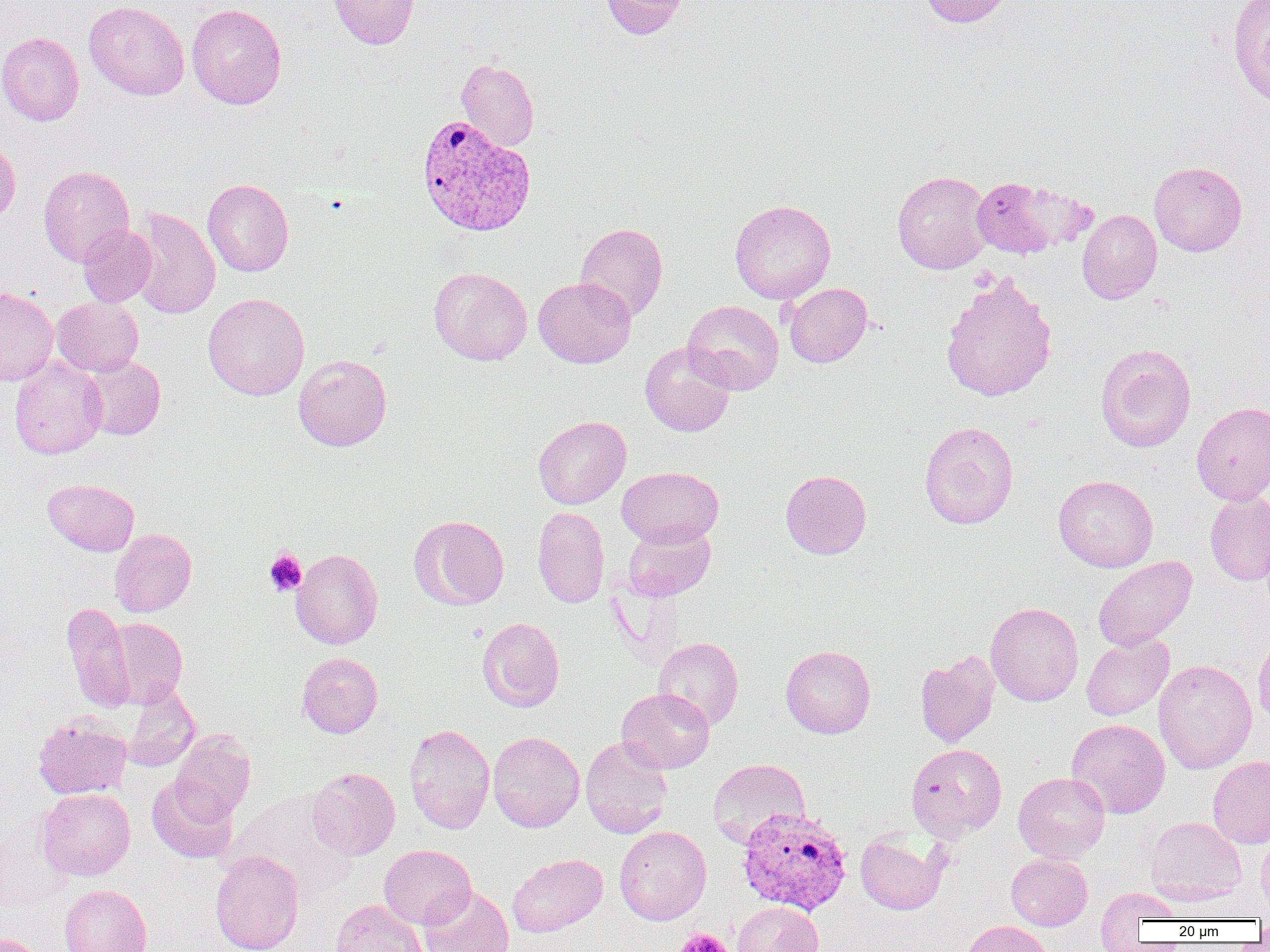
slide_level_diagnosis: Plasmodium vivax
magnification: 1000x
image_size: 1270×952 pixels
modality: optical microscopy
preparation: thin blood film
plasmodium_vivax_infected_red_blood_cell_locations: 'approximate bounding boxes as [x1, y1, x2, y2] in pixels: [416, 115, 536, 236], [737, 808, 853, 916]'
platelet_locations: 'approximate bounding boxes as [x1, y1, x2, y2] in pixels: [264, 549, 307, 596], [675, 928, 732, 952]'
uninfected_red_blood_cell_locations: 'approximate bounding boxes as [x1, y1, x2, y2] in pixels: [328, 0, 419, 49], [599, 0, 689, 39], [919, 0, 1014, 28], [1228, 0, 1270, 109], [83, 1, 190, 100], [186, 3, 286, 109], [0, 32, 84, 126], [456, 57, 539, 151], [0, 138, 20, 226], [1149, 161, 1247, 256], [38, 165, 134, 266], [892, 170, 992, 274], [967, 175, 1094, 260], [203, 179, 294, 277], [729, 199, 836, 304], [129, 206, 220, 320], [1077, 209, 1162, 304], [575, 223, 668, 322], [78, 225, 157, 307], [429, 267, 532, 365], [939, 272, 1058, 403], [533, 277, 636, 368], [784, 283, 872, 368], [0, 287, 58, 386], [203, 293, 310, 400], [52, 297, 143, 377], [683, 300, 784, 395], [640, 342, 736, 437], [1095, 343, 1196, 453], [293, 354, 392, 451], [9, 355, 107, 459], [81, 355, 165, 440], [1191, 401, 1270, 505], [533, 415, 631, 509], [919, 421, 1018, 529], [617, 466, 723, 547], [780, 470, 871, 559], [1053, 475, 1158, 572], [43, 478, 139, 555], [1205, 492, 1270, 585], [533, 506, 609, 608], [409, 515, 509, 610], [622, 522, 716, 601], [109, 528, 196, 617], [291, 549, 383, 649], [1092, 556, 1197, 651], [61, 602, 135, 712], [985, 602, 1083, 706], [105, 617, 188, 708], [478, 617, 564, 712], [1253, 627, 1270, 728], [1081, 633, 1174, 720], [653, 636, 744, 730], [781, 645, 875, 738], [915, 650, 1000, 748], [297, 652, 383, 738], [1153, 659, 1257, 774], [122, 685, 201, 771], [616, 688, 714, 773], [33, 715, 132, 799], [1066, 718, 1170, 818], [404, 723, 495, 834], [170, 729, 255, 823], [488, 731, 584, 833], [580, 736, 673, 838], [906, 743, 1007, 839], [1208, 755, 1270, 849], [707, 758, 810, 849], [307, 767, 400, 860], [1013, 772, 1110, 863], [146, 777, 238, 864], [38, 788, 135, 880], [230, 793, 356, 899], [1145, 816, 1247, 904], [0, 818, 74, 912], [614, 826, 711, 925], [1256, 827, 1270, 913], [855, 831, 948, 915], [379, 845, 476, 929], [210, 850, 304, 952], [507, 853, 608, 937], [1006, 853, 1092, 930], [60, 884, 152, 952], [418, 886, 515, 952], [1095, 886, 1182, 947], [330, 898, 427, 952], [732, 901, 823, 952], [962, 920, 1054, 952], [0, 933, 48, 952]'
field_of_view: one of a larger specimen